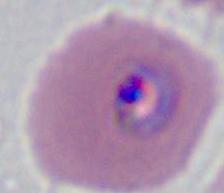

modality = photomicrograph
identification = Plasmodium
magnification = 400x or 1000x